Evaluate for malaria.
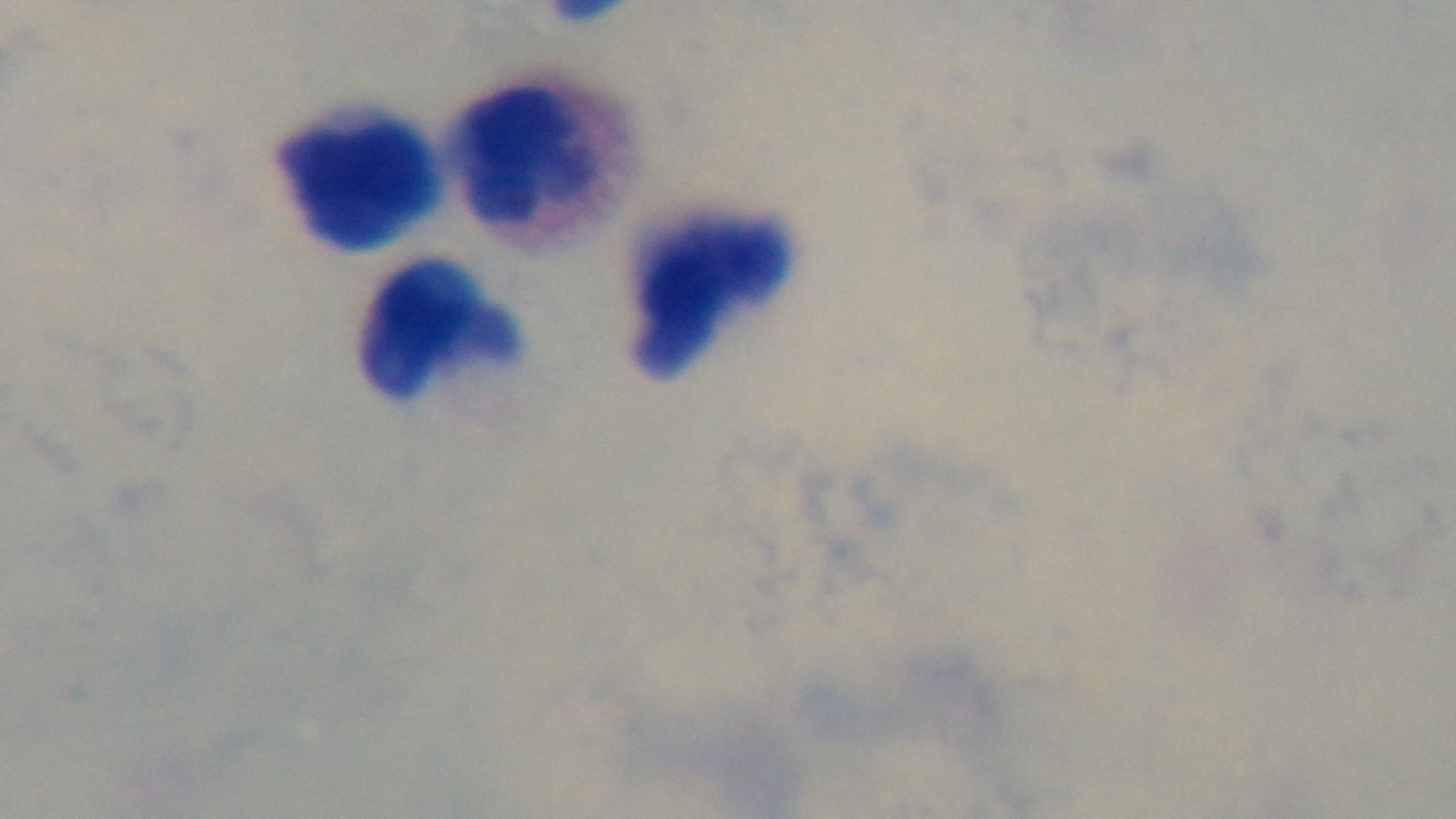

Uninfected.

100x oil-immersion objective. Giemsa-stained. Preparation: thick. Captured with a mounted 4K digital camera. Photomicrograph. One field from the slide.